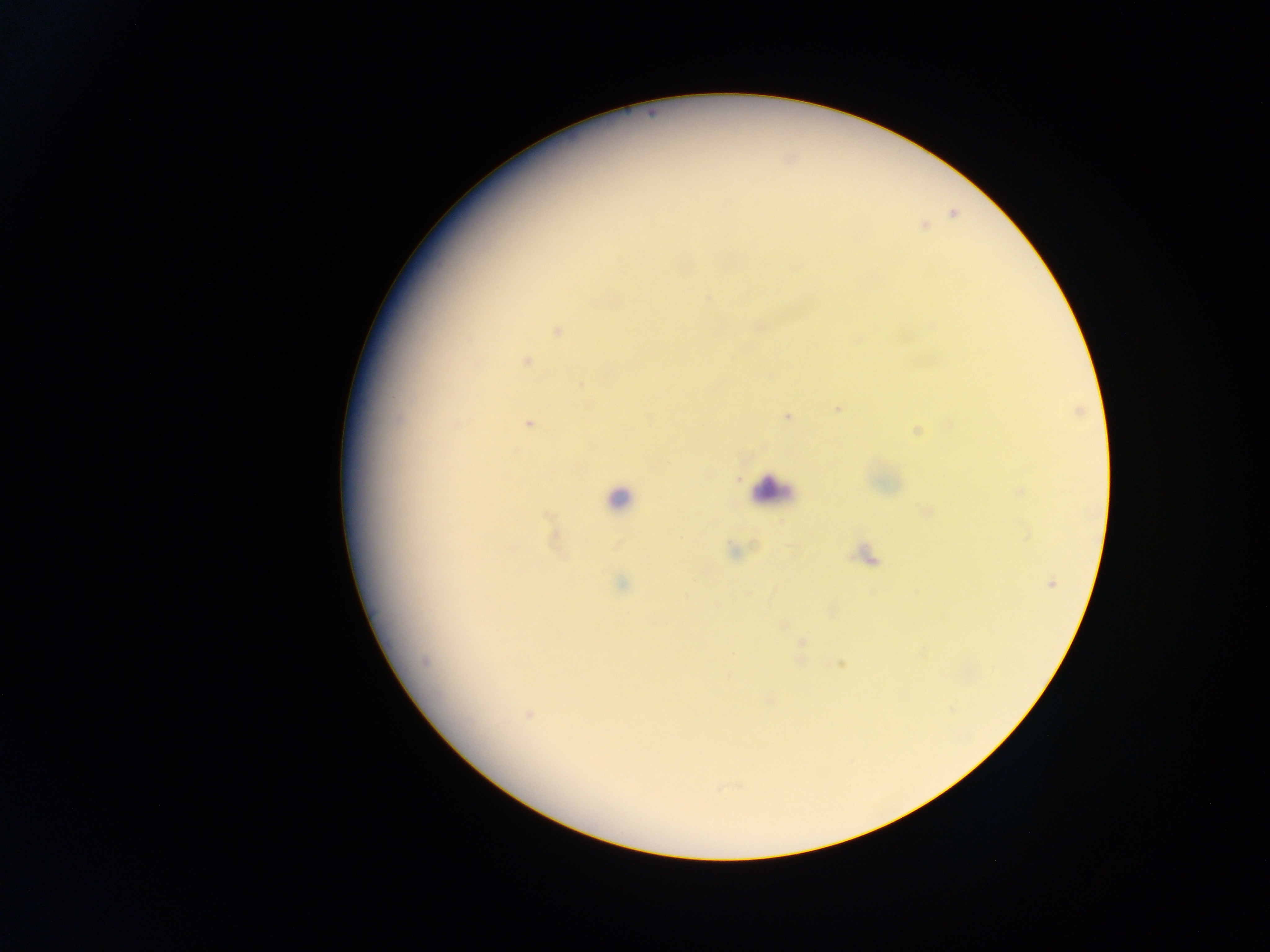
Approximate centers as (x, y) in pixels.
Summary:
  - Leukocyte locations: (772, 490), (618, 498)
  - Malaria parasite locations: (953, 213), (923, 226), (707, 297), (758, 326), (931, 326), (558, 330), (526, 360), (581, 385), (837, 408), (788, 416), (528, 423), (917, 431), (739, 479), (1020, 491), (926, 512), (555, 534), (733, 550), (866, 555), (1051, 582), (620, 583), (782, 625), (802, 643), (424, 662), (840, 662), (528, 714)
  - Image size: 1270×952 pixels
  - Preparation: thick blood film
  - Country: Ghana
  - Capture: mobile-phone photograph through a microscope
  - Field of view: single